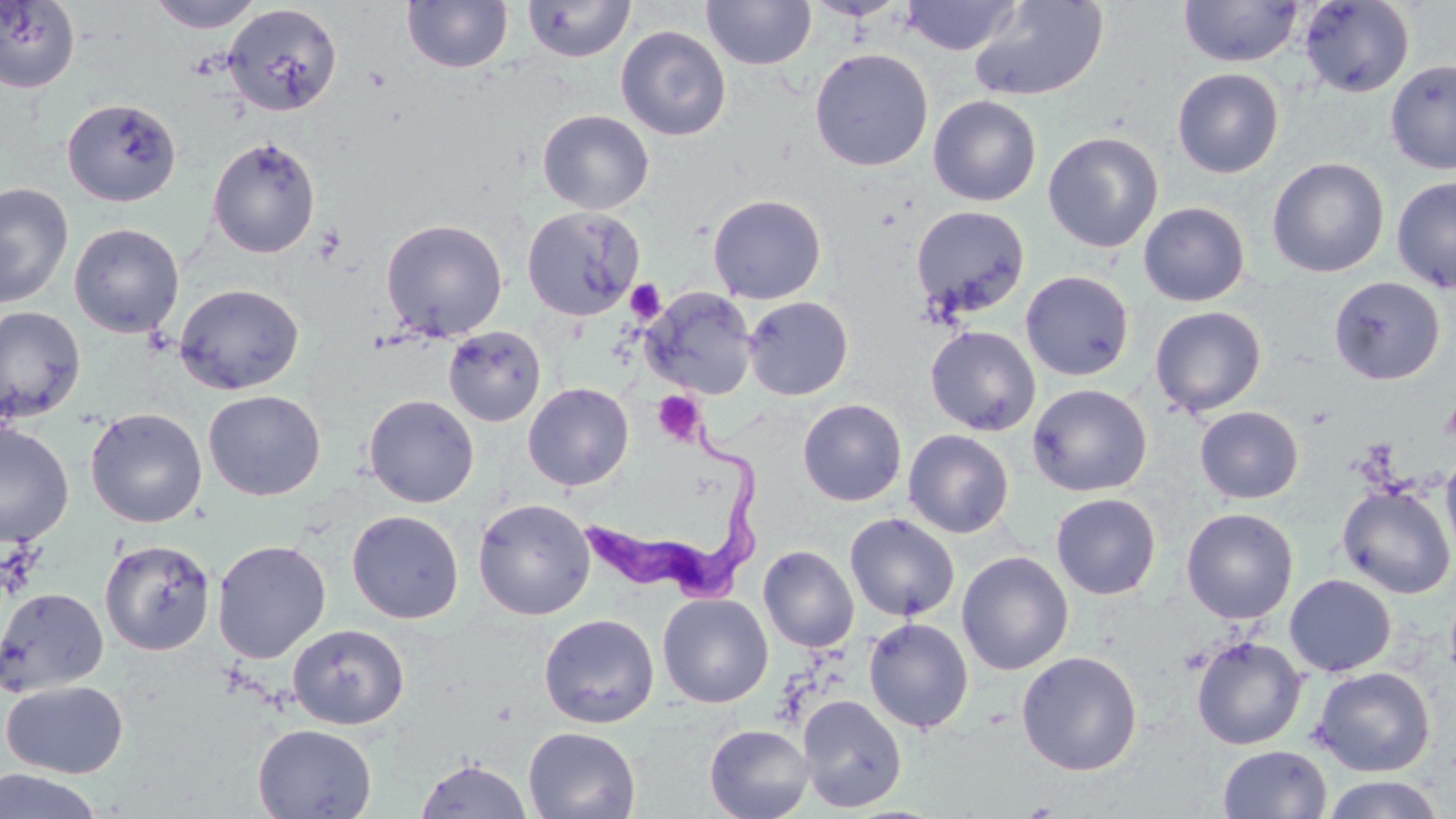

slide-level diagnosis = Trypanosoma brucei
uninfected red blood cell locations = approximate bounding boxes as [x1, y1, x2, y2] in pixels: [148, 0, 264, 32], [402, 0, 513, 73], [522, 0, 636, 62], [701, 0, 817, 70], [807, 0, 907, 21], [899, 0, 1022, 55], [1178, 0, 1304, 67], [1299, 0, 1415, 98], [0, 1, 81, 94], [969, 1, 1109, 101], [223, 4, 343, 116], [615, 25, 732, 141], [809, 48, 933, 171], [1385, 59, 1456, 174], [1172, 68, 1284, 178], [928, 95, 1042, 206], [62, 98, 182, 207], [537, 109, 654, 214], [1043, 131, 1164, 253], [207, 136, 321, 258], [1267, 156, 1389, 278], [1392, 176, 1456, 292], [0, 182, 74, 308], [707, 193, 827, 304], [1138, 201, 1250, 306], [521, 205, 644, 321], [910, 205, 1030, 318], [380, 218, 508, 341], [68, 222, 184, 338], [1020, 270, 1135, 381], [1328, 276, 1445, 385], [174, 283, 304, 395], [640, 287, 757, 399], [743, 295, 854, 400], [0, 305, 86, 424], [1149, 306, 1267, 417], [924, 325, 1041, 436], [443, 326, 547, 426], [523, 382, 634, 491], [1027, 383, 1152, 497], [203, 390, 325, 500], [363, 394, 479, 508], [797, 398, 907, 506], [1194, 406, 1304, 503], [85, 407, 207, 528], [0, 422, 74, 547], [903, 429, 1014, 538], [1440, 451, 1456, 564], [1336, 483, 1456, 599], [1050, 493, 1161, 600], [473, 498, 595, 620], [1181, 507, 1298, 624], [347, 510, 464, 624], [845, 513, 960, 621], [100, 539, 215, 655], [212, 539, 331, 663], [758, 544, 859, 652], [956, 551, 1074, 675], [1284, 574, 1396, 676], [0, 587, 109, 697], [657, 593, 773, 708], [539, 613, 659, 728], [863, 617, 974, 734], [287, 623, 409, 730], [1190, 635, 1308, 750], [1016, 651, 1142, 776], [1311, 666, 1435, 776], [1, 680, 128, 778], [797, 694, 907, 813], [252, 724, 378, 818], [705, 724, 814, 819], [523, 726, 641, 819], [1217, 744, 1332, 819], [414, 757, 533, 819], [1, 770, 106, 819], [1321, 775, 1446, 818]
stain = May-Grünwald-Giemsa
preparation = thin blood film
image size = 1456×819 pixels
modality = optical microscopy
field of view = single
Trypanosoma brucei locations = approximate bounding boxes as [x1, y1, x2, y2] in pixels: [583, 422, 760, 609]
platelet locations = approximate bounding boxes as [x1, y1, x2, y2] in pixels: [627, 281, 665, 324], [653, 391, 705, 446]
magnification = 1000x